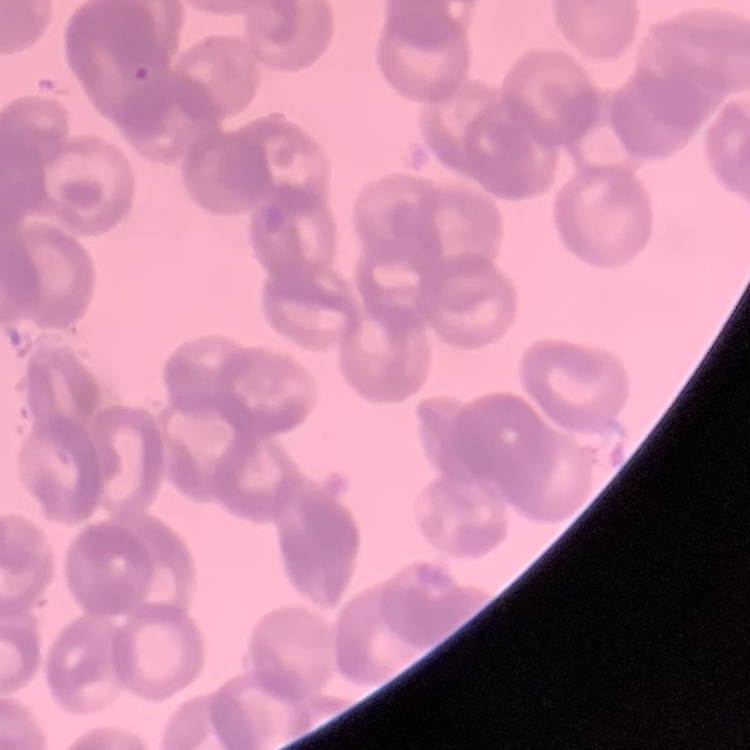 The red blood cells show rouleaux formation. Thin blood film. Field's or Giemsa stain. Square crop of a larger photomicrograph.